Identify the cell.
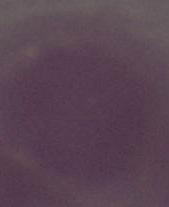

An erythrocyte.

{
  "modality": "photomicrograph",
  "magnification": "1000x"
}